Assess this cell for malaria.
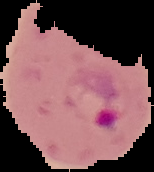
It is parasitized.

From a thin blood smear. Image is 154×172 pixels. Segmented cell region on a black background.